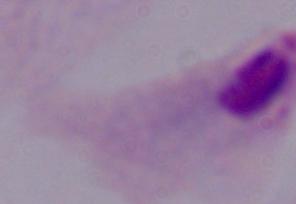
Captured at 1000x magnification. A trichomonad is seen. Photomicrograph.